Give the position of every leukocyte visible.
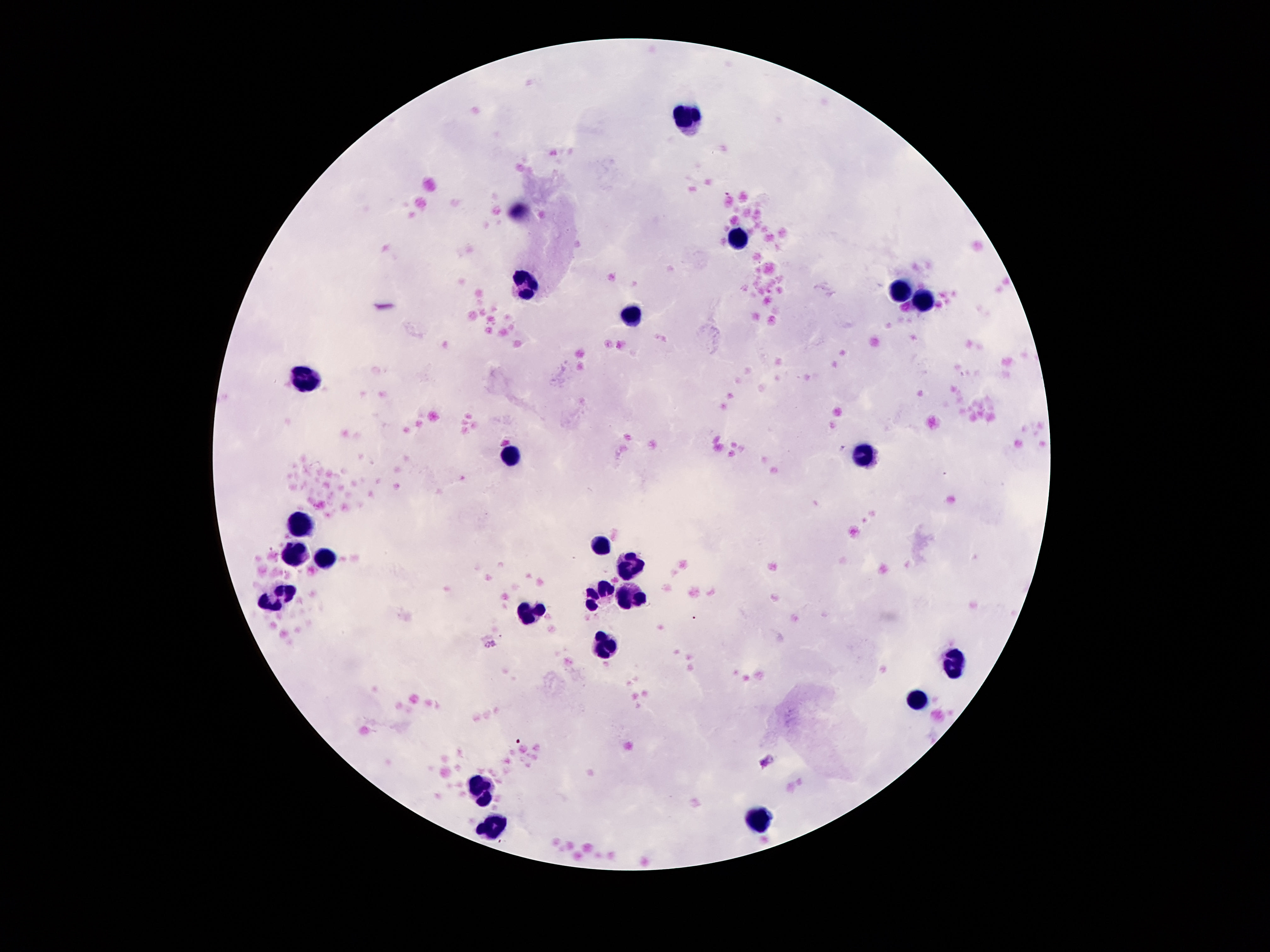

Approximate centers as (x, y) in pixels.
Leukocytes: (687, 114), (737, 238), (527, 284), (903, 290), (925, 301), (633, 314), (305, 379), (865, 452), (509, 455), (299, 522), (601, 544), (293, 552), (327, 558), (627, 568), (281, 594), (597, 594), (635, 598), (529, 612), (603, 648), (952, 662), (917, 702), (481, 788), (763, 819), (493, 823).

Image is 1270×952 pixels. Thick blood film. Single field of view. Smartphone photograph taken through the microscope eyepiece. 100x magnification. Giemsa-stained preparation. Patient malaria status: negative.